Assess this cell for malaria.
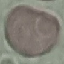
Uninfected.

image type = cell patch, automatically extracted from a larger field of view and resized to 64 × 64 pixels
capture = smartphone through the microscope eyepiece
stain = Giemsa
preparation = thin smear